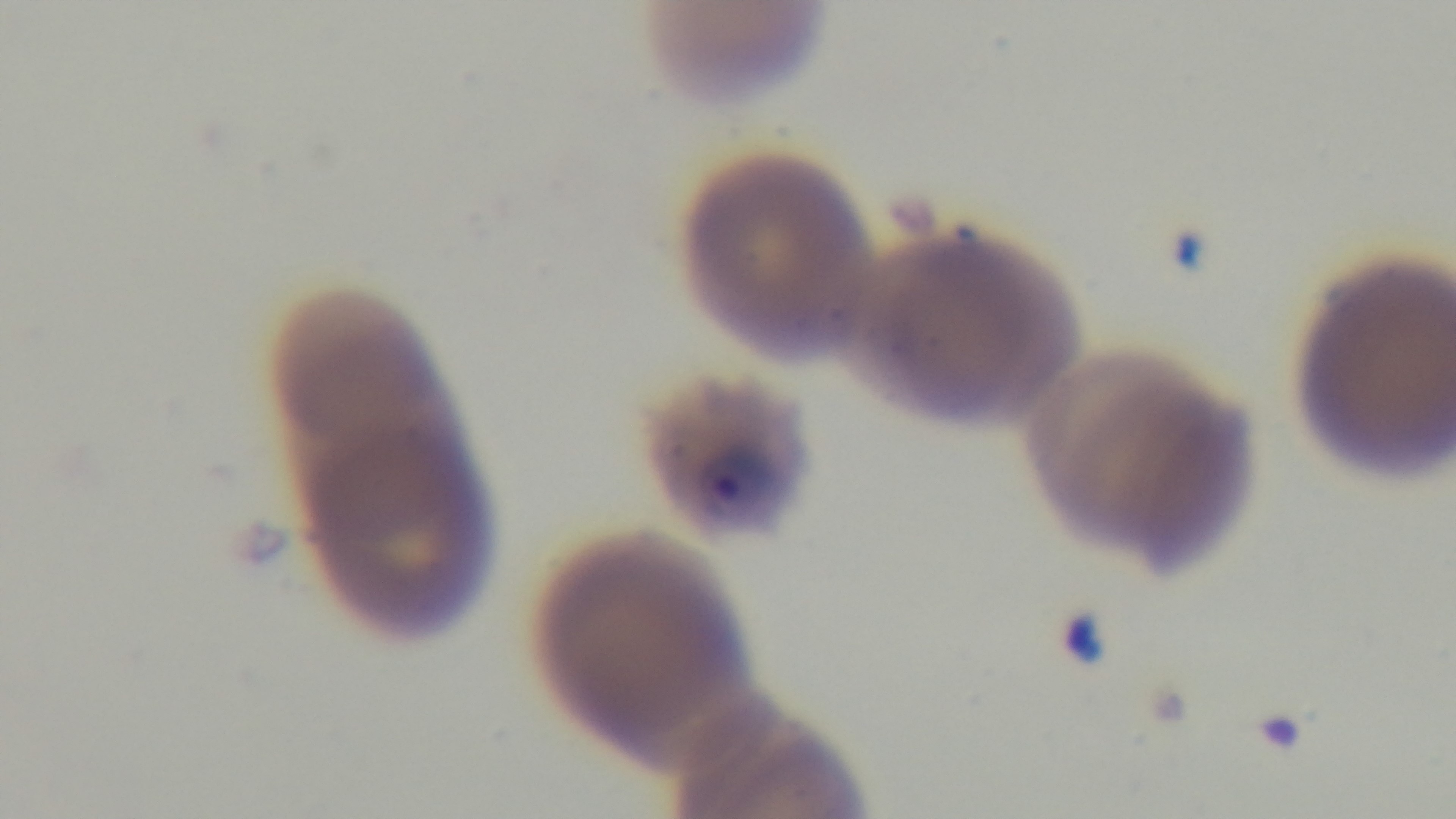
Giemsa-stained. Single field of view. Malaria status: infected. Mounted 4K digital camera. Light microscopy. Preparation: thin blood film. 100x oil-immersion objective.